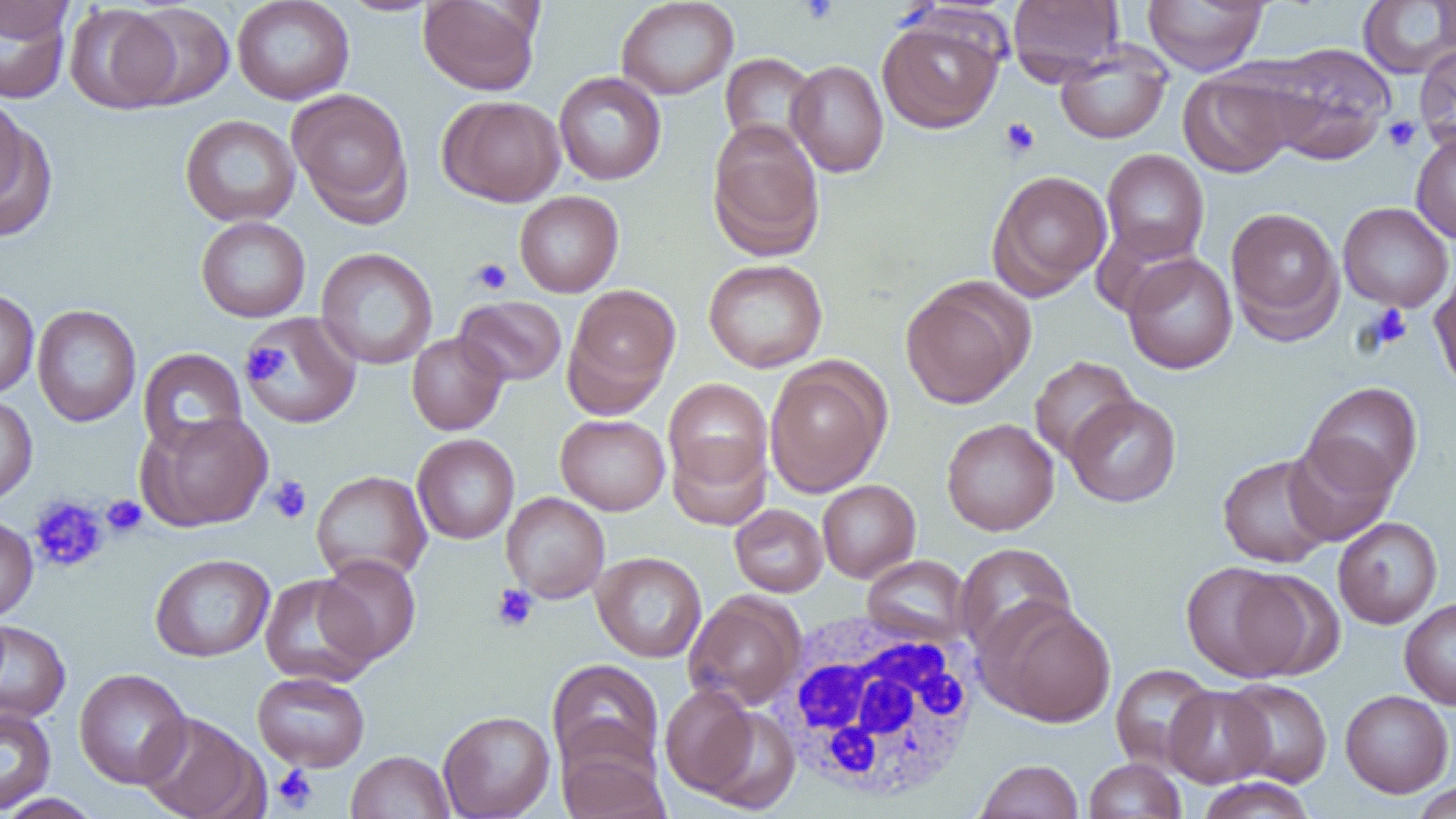
slide-level diagnosis = negative for blood parasites
magnification = 1000x
image size = 1456×819 pixels
uninfected red blood cell locations = approximate bounding boxes as (x1,y1)-(x2,y2) corner pairs in pixels: (0,0)-(74,42), (232,0)-(355,105), (338,0)-(442,17), (418,0)-(542,96), (616,0)-(739,100), (1007,0)-(1125,85), (1143,0)-(1268,75), (1358,0)-(1456,78), (0,1)-(73,104), (65,3)-(181,114), (120,3)-(235,109), (876,13)-(1006,134), (1055,41)-(1172,145), (1258,42)-(1396,163), (1414,43)-(1456,149), (720,52)-(821,155), (788,60)-(889,178), (1179,70)-(1296,178), (553,72)-(667,185), (286,88)-(414,225), (0,95)-(29,208), (439,95)-(565,207), (0,109)-(55,240), (179,114)-(301,226), (707,123)-(825,262), (1411,132)-(1456,244), (1101,149)-(1210,262), (986,169)-(1112,300), (514,191)-(624,297), (1338,202)-(1454,312), (1225,206)-(1344,342), (195,216)-(310,322), (315,247)-(438,370), (1122,253)-(1238,374), (703,258)-(828,372), (1430,268)-(1456,395), (899,278)-(1032,409), (563,284)-(681,414), (0,287)-(39,400), (455,295)-(567,386), (32,304)-(141,426), (243,311)-(362,428), (406,332)-(509,436), (137,347)-(248,454), (1029,356)-(1138,463), (764,358)-(890,497), (663,378)-(773,493), (1302,382)-(1423,495), (1064,394)-(1181,507), (0,395)-(37,507), (139,411)-(273,531), (555,414)-(670,515), (941,417)-(1059,535), (412,433)-(520,544), (668,434)-(771,531), (1283,437)-(1397,545), (1218,454)-(1335,568), (311,469)-(432,585), (817,479)-(920,582), (501,492)-(610,603), (730,504)-(828,597), (0,516)-(38,622), (1333,517)-(1442,629), (954,542)-(1077,658), (591,551)-(707,662), (150,553)-(275,662), (316,554)-(421,664), (861,555)-(972,646), (1181,561)-(1312,683), (259,573)-(379,686), (683,591)-(806,711), (1399,598)-(1456,709), (980,600)-(1117,727), (0,620)-(71,724), (547,659)-(664,777), (1110,663)-(1217,772), (74,668)-(192,789), (252,671)-(370,771), (1220,678)-(1333,788), (659,683)-(760,799), (1164,686)-(1274,787), (1340,690)-(1454,797), (695,703)-(800,814), (0,706)-(56,814), (438,710)-(555,818), (138,712)-(264,819), (557,740)-(670,819), (345,750)-(454,819), (1084,758)-(1186,818), (974,759)-(1083,819), (1196,778)-(1316,819), (1410,781)-(1456,819), (0,793)-(104,818)
platelet locations = approximate bounding boxes as (x1,y1)-(x2,y2) corner pairs in pixels: (799,0)-(838,24), (1383,115)-(1421,152), (1000,117)-(1040,159), (470,258)-(513,295), (1364,304)-(1412,351), (243,341)-(289,386), (266,476)-(312,524), (28,495)-(108,573), (101,495)-(147,538), (492,584)-(538,632), (272,764)-(318,812)
modality = light microscopy
white blood cell locations = approximate bounding boxes as (x1,y1)-(x2,y2) corner pairs in pixels: (769,610)-(985,805)
field of view = one of a larger specimen
preparation = thin blood smear